Mark where platelets are.
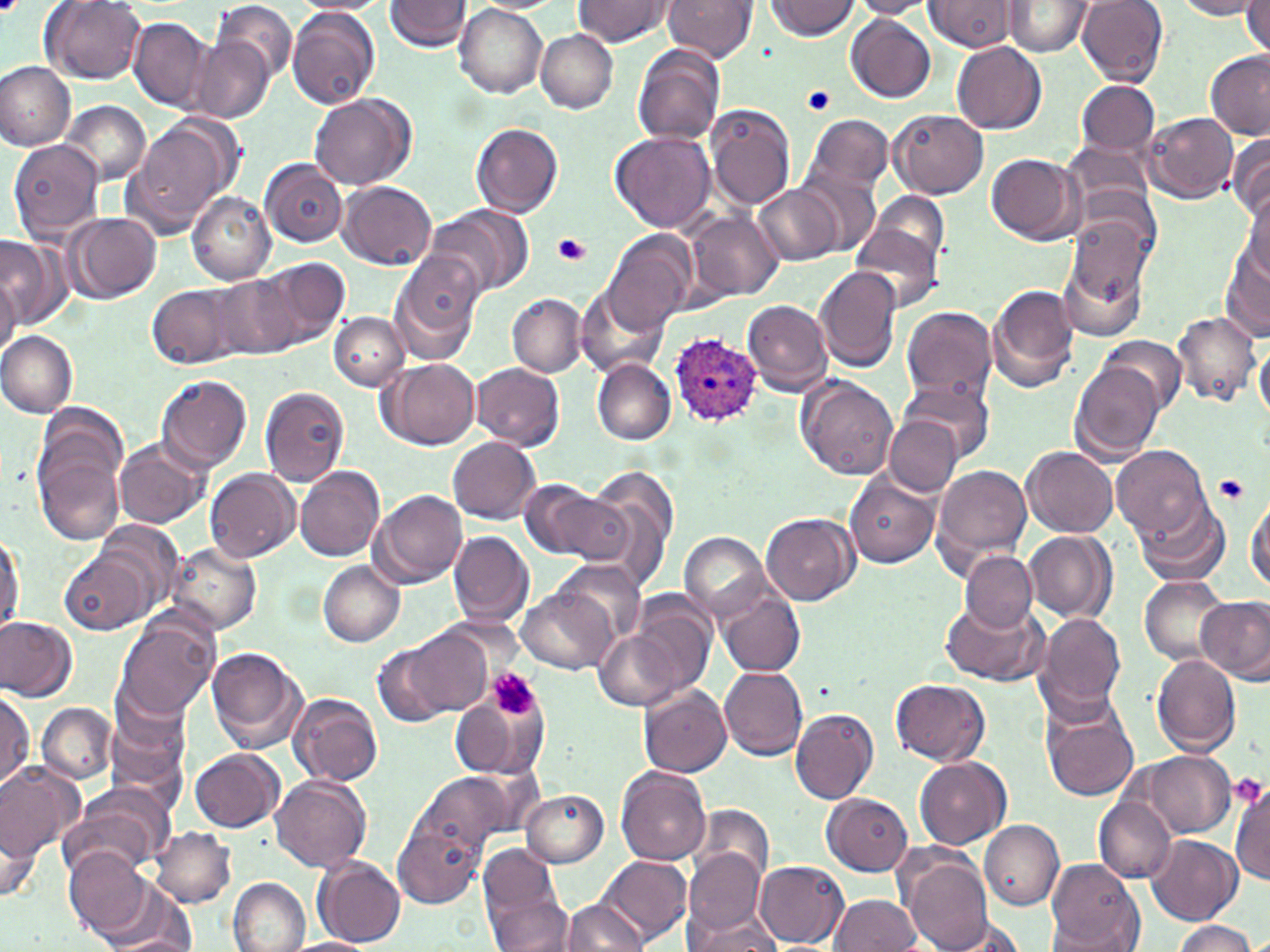
Approximate bounding boxes as (x1, y1, x2, y2) in pixels.
Platelets: (802, 86, 836, 116), (552, 233, 590, 266), (1216, 473, 1249, 503), (489, 669, 541, 720), (1230, 773, 1267, 806).

Summary:
  - Uninfected red blood cell locations: (213, 0, 298, 83), (292, 0, 391, 15), (386, 0, 472, 52), (661, 0, 756, 62), (767, 0, 860, 41), (848, 0, 938, 19), (922, 0, 1023, 52), (1173, 0, 1267, 20), (1242, 0, 1270, 61), (40, 1, 148, 84), (574, 1, 671, 47), (1002, 2, 1095, 56), (1077, 2, 1168, 85), (457, 4, 547, 99), (287, 7, 381, 109), (847, 14, 937, 103), (129, 17, 214, 113), (535, 30, 618, 112), (191, 38, 273, 124), (951, 41, 1048, 134), (632, 46, 725, 148), (1203, 49, 1270, 139), (0, 61, 76, 150), (1073, 79, 1160, 159), (309, 93, 415, 190), (62, 100, 151, 185), (705, 105, 797, 209), (888, 108, 989, 199), (803, 114, 892, 198), (1144, 114, 1239, 203), (122, 118, 239, 236), (471, 122, 564, 217), (611, 132, 715, 234), (1227, 134, 1270, 223), (1060, 139, 1155, 218), (8, 140, 104, 241), (986, 152, 1085, 245), (259, 157, 346, 247), (797, 168, 882, 255), (341, 182, 437, 271), (753, 184, 844, 266), (1240, 186, 1270, 284), (187, 190, 275, 284), (870, 191, 949, 269), (430, 205, 535, 297), (1066, 205, 1158, 308), (686, 210, 783, 301), (65, 212, 160, 303), (850, 220, 943, 316), (603, 229, 697, 336), (0, 235, 69, 328), (1219, 239, 1270, 340), (1056, 240, 1151, 343), (391, 251, 484, 360), (261, 255, 352, 346), (0, 265, 20, 357), (814, 267, 902, 374), (211, 274, 305, 363), (146, 281, 247, 369), (986, 284, 1080, 392), (577, 291, 667, 378), (507, 294, 586, 378), (742, 300, 833, 396), (901, 306, 998, 404), (329, 311, 409, 390), (1171, 311, 1260, 410), (0, 333, 78, 417), (1100, 337, 1188, 414), (1254, 338, 1270, 422), (378, 357, 481, 449), (592, 358, 675, 444), (1069, 359, 1164, 463), (472, 363, 565, 449), (156, 374, 251, 471), (799, 376, 899, 481), (898, 380, 996, 461), (260, 386, 349, 485), (38, 402, 129, 495), (886, 417, 961, 495), (448, 437, 540, 523), (32, 438, 127, 544), (112, 438, 210, 529), (1111, 443, 1211, 543), (1024, 446, 1119, 539), (932, 464, 1034, 571), (295, 466, 385, 561), (582, 467, 679, 582), (205, 468, 300, 562), (846, 473, 940, 567), (518, 478, 599, 558), (373, 488, 468, 586), (1247, 488, 1270, 597), (537, 490, 634, 565), (1132, 494, 1232, 589), (761, 512, 858, 605), (93, 519, 184, 619), (0, 529, 25, 634), (447, 530, 533, 627), (1024, 530, 1116, 624), (680, 531, 770, 622), (168, 542, 262, 637), (961, 552, 1037, 633), (61, 554, 145, 635), (555, 559, 647, 645), (317, 561, 405, 647), (1138, 574, 1227, 665), (516, 585, 617, 673), (716, 588, 806, 677), (1197, 594, 1270, 684), (941, 599, 1045, 686), (633, 600, 715, 695), (117, 613, 219, 722), (1035, 614, 1127, 713), (0, 616, 78, 702), (595, 623, 695, 712), (392, 627, 492, 719), (374, 641, 457, 729), (205, 646, 308, 752), (1152, 654, 1242, 757), (720, 666, 808, 760), (890, 678, 990, 765), (638, 685, 732, 777), (1, 689, 34, 792), (449, 691, 542, 786), (290, 692, 383, 786), (106, 693, 191, 799), (1040, 699, 1141, 802), (36, 702, 117, 784), (789, 708, 878, 804), (189, 748, 284, 832), (1138, 752, 1236, 837), (914, 756, 1011, 849), (0, 761, 85, 862), (615, 768, 711, 866), (411, 772, 510, 865), (270, 775, 371, 872), (1231, 780, 1270, 886), (61, 785, 172, 878), (521, 788, 609, 867), (822, 792, 913, 875), (1092, 796, 1175, 882), (691, 803, 775, 891), (2, 815, 42, 905), (979, 820, 1064, 908), (394, 821, 483, 910), (151, 827, 235, 907), (1148, 835, 1243, 924), (64, 847, 154, 941), (684, 849, 766, 934), (479, 851, 570, 951), (313, 854, 407, 947), (597, 855, 692, 947), (900, 855, 992, 952), (756, 859, 849, 948), (1044, 862, 1145, 950), (229, 877, 310, 952), (96, 880, 195, 951), (830, 894, 922, 951), (560, 897, 649, 951), (683, 906, 781, 951), (932, 914, 1032, 951), (1170, 921, 1260, 952), (282, 938, 375, 952)
  - Plasmodium ovale-infected red blood cell locations: (670, 335, 764, 424)
  - Slide-level diagnosis: Plasmodium ovale
  - Stain: May-Grünwald-Giemsa
  - Magnification: 1000x
  - Preparation: thin blood film
  - Image size: 1270×952 pixels
  - Field of view: single
  - Modality: light microscopy